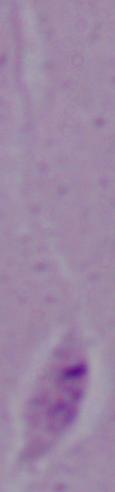
Summary:
  - Magnification: 1000x
  - Identification: Leishmania
  - Modality: photomicrograph